Report the malaria status of this cell.
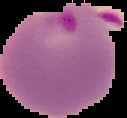
Parasitized.

Summary:
  - Image size: 127×118 pixels
  - Preparation: thin blood smear
  - Image type: cell region segmented out of the field of view; surrounding area masked to black